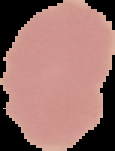 The area outside the segmented cell region is set to black. From a thin blood film. Malaria status: uninfected. Image is 115×151 pixels.